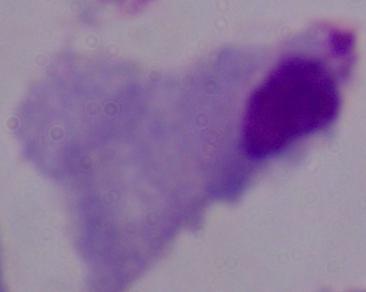
Summary:
  - Identification: trichomonad
  - Modality: photomicrograph
  - Magnification: 1000x